State which parasite is depicted.
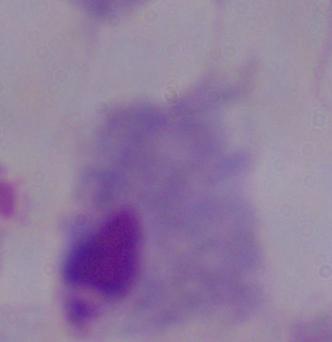
This is a trichomonad.

modality = photomicrograph
magnification = 1000x